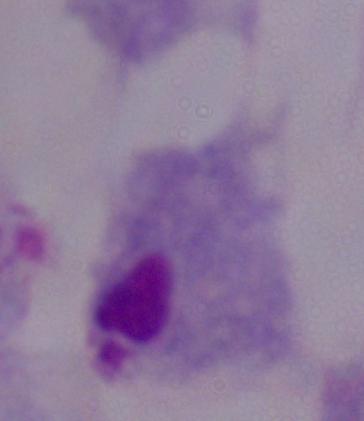

modality = micrograph
identification = trichomonad
magnification = 1000x